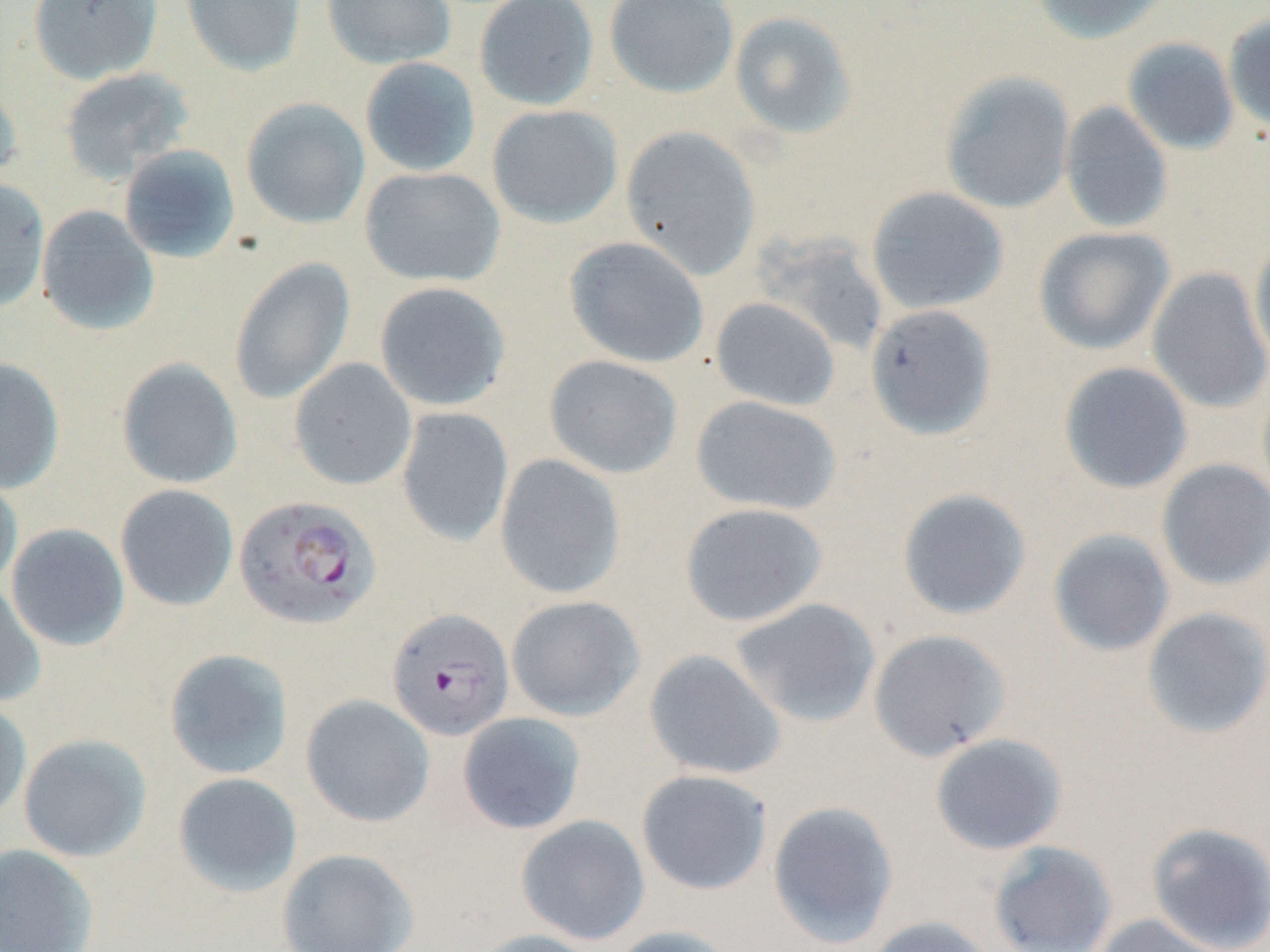
Summary:
  - Coordinate format: approximate bounding boxes as [x1, y1, x2, y2] in pixels
  - Plasmodium falciparum-infected red blood cell locations: [234, 495, 382, 630], [386, 607, 514, 741]
  - Uninfected red blood cell locations: [27, 0, 163, 84], [181, 0, 307, 76], [321, 0, 456, 69], [474, 0, 599, 111], [604, 0, 739, 99], [1032, 0, 1173, 44], [728, 10, 858, 139], [1223, 14, 1270, 134], [1121, 37, 1239, 155], [359, 56, 481, 178], [60, 68, 194, 184], [939, 71, 1076, 215], [0, 76, 23, 190], [241, 98, 370, 229], [1059, 101, 1173, 233], [487, 104, 623, 228], [620, 125, 761, 280], [118, 144, 241, 264], [360, 166, 505, 287], [0, 179, 50, 312], [866, 186, 1009, 315], [36, 205, 159, 336], [1033, 226, 1175, 355], [1249, 235, 1270, 370], [564, 236, 709, 368], [228, 258, 356, 405], [1147, 266, 1270, 414], [374, 281, 511, 411], [710, 297, 840, 411], [865, 304, 998, 441], [544, 354, 683, 479], [0, 357, 64, 493], [116, 357, 243, 489], [289, 358, 417, 491], [1058, 361, 1194, 494], [691, 395, 842, 515], [396, 407, 514, 547], [495, 454, 626, 600], [1155, 459, 1270, 591], [0, 470, 23, 593], [115, 484, 239, 611], [896, 487, 1033, 621], [678, 502, 828, 627], [6, 524, 130, 651], [1048, 528, 1175, 657], [0, 579, 46, 708], [506, 595, 645, 721], [730, 598, 881, 728], [1141, 607, 1270, 740], [868, 628, 1012, 762], [163, 648, 294, 780], [644, 649, 787, 781], [301, 694, 435, 828], [0, 699, 32, 824], [457, 712, 586, 835], [18, 733, 152, 862], [930, 733, 1069, 855], [635, 769, 773, 895], [172, 772, 302, 897], [767, 800, 899, 947], [515, 814, 650, 945], [1146, 821, 1270, 952], [989, 842, 1119, 952], [0, 843, 99, 951], [276, 848, 419, 952], [1090, 913, 1229, 952], [865, 916, 996, 952], [607, 925, 735, 952], [470, 928, 605, 952]
  - Slide-level diagnosis: Plasmodium falciparum
  - Modality: light microscopy
  - Stain: May-Grünwald-Giemsa
  - Image size: 1270×952 pixels
  - Preparation: thin blood film
  - Field of view: one of a larger specimen
  - Magnification: 1000x